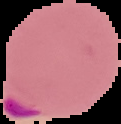
malaria_status: parasitized
image_size: 121×124 pixels
image_type: cell region segmented out of the field of view; surrounding area masked to black
preparation: thin blood smear